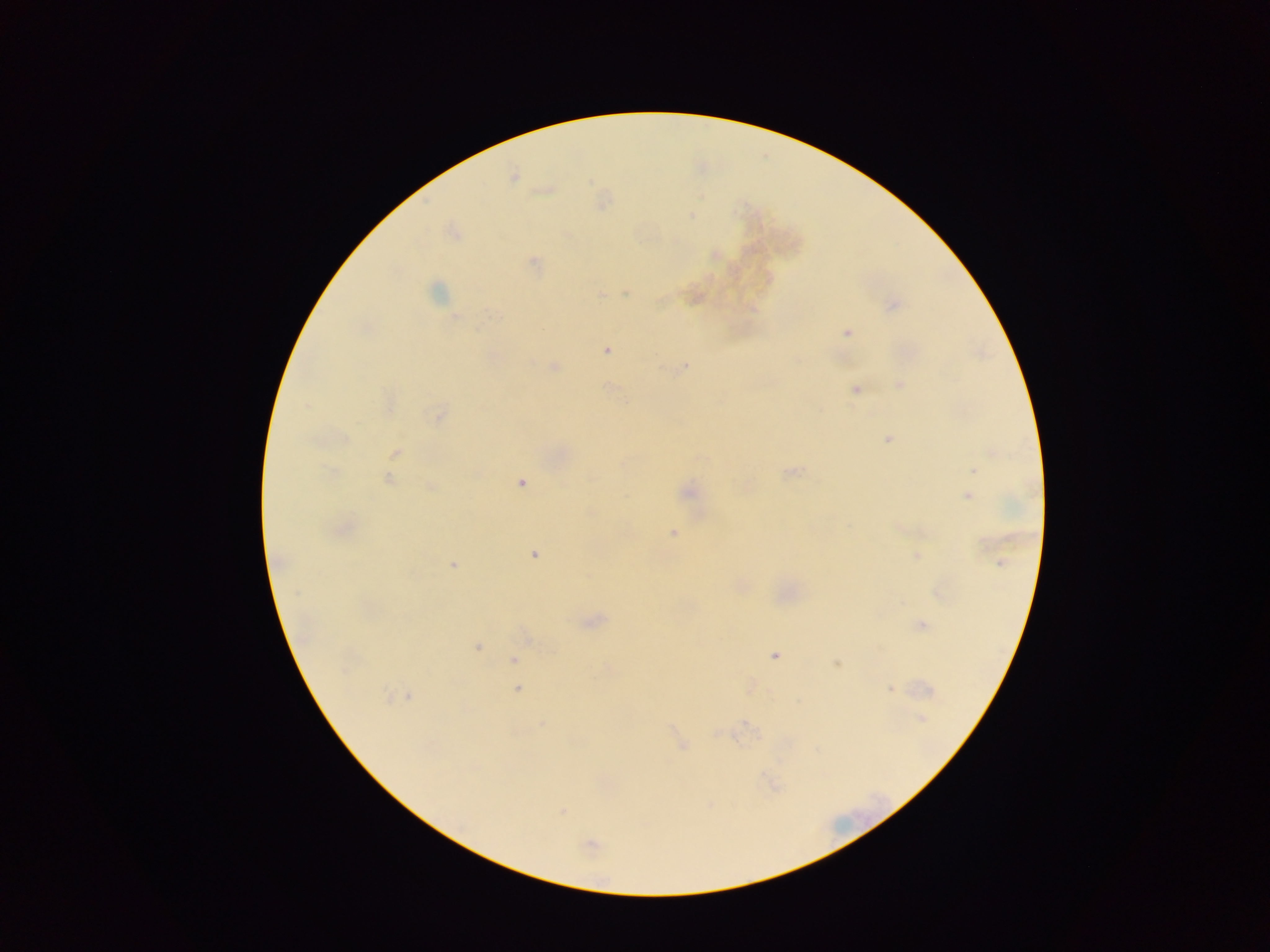
{
  "preparation": "thick blood film",
  "image_size": "1270×952 pixels",
  "capture": "mobile-phone photograph through a microscope",
  "field_of_view": "single",
  "malaria_parasite_locations": "approximate centers as {x, y} in pixels: {513, 176}, {691, 216}, {533, 263}, {436, 291}, {626, 293}, {601, 295}, {893, 305}, {456, 318}, {847, 333}, {606, 350}, {554, 366}, {684, 367}, {900, 385}, {856, 390}, {306, 406}, {439, 415}, {345, 438}, {888, 439}, {396, 452}, {973, 470}, {791, 472}, {388, 479}, {522, 483}, {430, 487}, {688, 492}, {967, 496}, {673, 533}, {534, 555}, {917, 556}, {1002, 562}, {453, 564}, {297, 593}, {921, 625}, {477, 647}, {774, 655}, {514, 660}, {837, 664}, {518, 689}, {890, 689}, {387, 695}, {410, 697}, {922, 718}, {542, 723}, {683, 747}, {563, 810}, {590, 845}",
  "country": "Ghana"
}